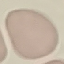

malaria status = uninfected
capture = smartphone camera at the microscope eyepiece
preparation = thin smear
image type = automatically extracted cell patch, resized to 64 × 64 pixels
stain = Giemsa